Report the malaria status of this cell.
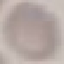
Uninfected.

preparation: thin smear
stain: Giemsa
capture: smartphone camera at the microscope eyepiece
image_type: automatically extracted cell patch, resized to 64 × 64 pixels